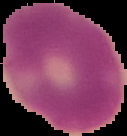

Summary:
  - Preparation: thin blood smear
  - Image type: cell region segmented out of the field of view; surrounding area masked to black
  - Image size: 127×136 pixels
  - Malaria status: uninfected